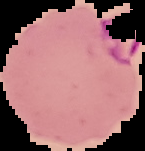

{
  "image_size": "145×151 pixels",
  "preparation": "thin blood film",
  "malaria_status": "parasitized",
  "image_type": "segmented cell region on a black background"
}